Outline each blood parasite and name the species.
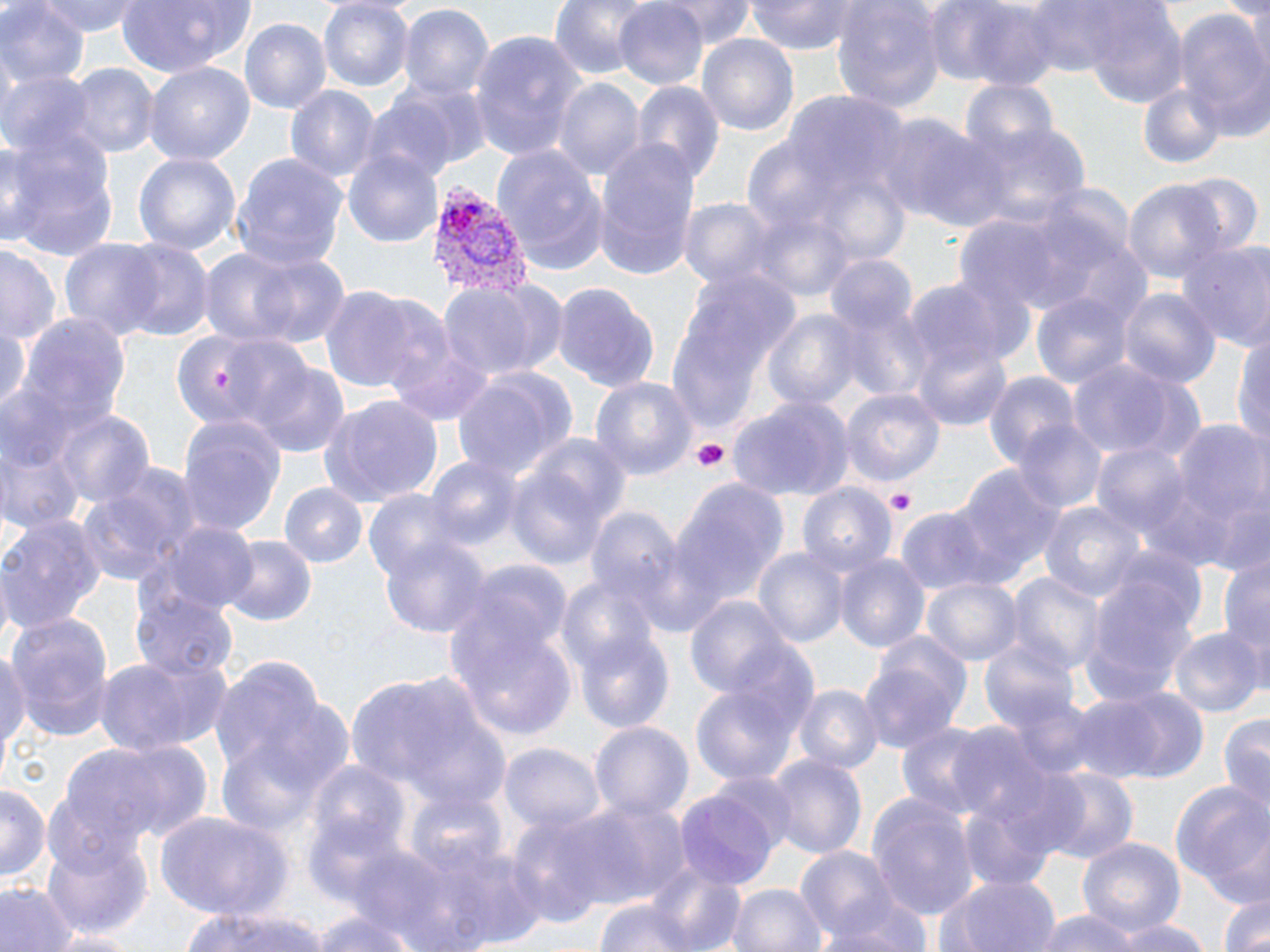
Approximate bounding boxes as named x1/y1/x2/y2 corners in pixels.
Plasmodium vivax-infected red blood cells: (x1=424, y1=182, x2=534, y2=306).
No Plasmodium falciparum, Plasmodium ovale, Plasmodium malariae, Babesia divergens, or Trypanosoma brucei observed.

Uninfected red blood cell locations: (x1=0, y1=0, x2=86, y2=95), (x1=40, y1=0, x2=142, y2=37), (x1=114, y1=0, x2=257, y2=78), (x1=549, y1=0, x2=665, y2=84), (x1=611, y1=0, x2=710, y2=91), (x1=657, y1=0, x2=757, y2=43), (x1=745, y1=0, x2=867, y2=52), (x1=831, y1=0, x2=945, y2=114), (x1=1019, y1=0, x2=1131, y2=77), (x1=1245, y1=0, x2=1269, y2=82), (x1=934, y1=1, x2=1063, y2=88), (x1=317, y1=2, x2=413, y2=91), (x1=399, y1=3, x2=494, y2=106), (x1=1082, y1=4, x2=1189, y2=111), (x1=1172, y1=8, x2=1270, y2=141), (x1=239, y1=17, x2=332, y2=115), (x1=469, y1=33, x2=585, y2=161), (x1=698, y1=33, x2=798, y2=141), (x1=145, y1=62, x2=255, y2=164), (x1=69, y1=66, x2=159, y2=157), (x1=0, y1=69, x2=95, y2=161), (x1=552, y1=77, x2=643, y2=182), (x1=960, y1=80, x2=1060, y2=162), (x1=632, y1=81, x2=724, y2=188), (x1=1135, y1=81, x2=1228, y2=172), (x1=287, y1=85, x2=380, y2=187), (x1=360, y1=96, x2=462, y2=185), (x1=875, y1=106, x2=1003, y2=232), (x1=962, y1=119, x2=1090, y2=229), (x1=0, y1=133, x2=123, y2=264), (x1=594, y1=140, x2=703, y2=281), (x1=492, y1=144, x2=611, y2=273), (x1=345, y1=150, x2=443, y2=250), (x1=134, y1=152, x2=241, y2=260), (x1=232, y1=153, x2=349, y2=271), (x1=1174, y1=172, x2=1263, y2=259), (x1=1122, y1=179, x2=1226, y2=285), (x1=677, y1=198, x2=776, y2=292), (x1=58, y1=239, x2=168, y2=337), (x1=115, y1=239, x2=213, y2=341), (x1=1174, y1=239, x2=1270, y2=352), (x1=201, y1=242, x2=344, y2=351), (x1=1, y1=243, x2=62, y2=350), (x1=664, y1=267, x2=804, y2=437), (x1=903, y1=275, x2=1031, y2=377), (x1=438, y1=281, x2=560, y2=382), (x1=550, y1=282, x2=661, y2=394), (x1=321, y1=287, x2=425, y2=397), (x1=1116, y1=288, x2=1220, y2=391), (x1=1032, y1=290, x2=1135, y2=393), (x1=764, y1=308, x2=867, y2=417), (x1=15, y1=314, x2=134, y2=445), (x1=0, y1=320, x2=32, y2=418), (x1=382, y1=327, x2=497, y2=428), (x1=1234, y1=330, x2=1270, y2=452), (x1=170, y1=333, x2=261, y2=428), (x1=221, y1=336, x2=316, y2=429), (x1=913, y1=341, x2=1014, y2=432), (x1=1065, y1=359, x2=1194, y2=460), (x1=250, y1=361, x2=350, y2=456), (x1=451, y1=369, x2=576, y2=483), (x1=987, y1=373, x2=1078, y2=471), (x1=591, y1=375, x2=697, y2=479), (x1=840, y1=387, x2=944, y2=486), (x1=317, y1=393, x2=442, y2=508), (x1=728, y1=394, x2=851, y2=500), (x1=53, y1=408, x2=155, y2=514), (x1=177, y1=413, x2=285, y2=537), (x1=1169, y1=416, x2=1270, y2=551), (x1=1012, y1=420, x2=1105, y2=515), (x1=1093, y1=440, x2=1194, y2=544), (x1=1, y1=445, x2=82, y2=534), (x1=424, y1=457, x2=521, y2=552), (x1=504, y1=459, x2=619, y2=575), (x1=79, y1=464, x2=204, y2=585), (x1=948, y1=465, x2=1063, y2=588), (x1=669, y1=474, x2=790, y2=616), (x1=799, y1=483, x2=895, y2=582), (x1=279, y1=484, x2=367, y2=568), (x1=363, y1=486, x2=463, y2=583), (x1=1038, y1=501, x2=1145, y2=608), (x1=588, y1=505, x2=682, y2=610), (x1=895, y1=507, x2=999, y2=595), (x1=0, y1=514, x2=108, y2=637), (x1=150, y1=519, x2=262, y2=614), (x1=377, y1=530, x2=494, y2=643), (x1=219, y1=536, x2=318, y2=628), (x1=753, y1=547, x2=848, y2=652), (x1=1220, y1=550, x2=1270, y2=668), (x1=835, y1=551, x2=929, y2=655), (x1=1079, y1=572, x2=1201, y2=709), (x1=1011, y1=574, x2=1102, y2=674), (x1=556, y1=575, x2=662, y2=686), (x1=923, y1=575, x2=1023, y2=666), (x1=131, y1=590, x2=237, y2=682), (x1=683, y1=595, x2=792, y2=705), (x1=6, y1=613, x2=116, y2=740), (x1=449, y1=616, x2=578, y2=741), (x1=977, y1=628, x2=1084, y2=753), (x1=1169, y1=629, x2=1262, y2=720), (x1=577, y1=630, x2=674, y2=731), (x1=863, y1=633, x2=972, y2=753), (x1=0, y1=649, x2=32, y2=774), (x1=92, y1=650, x2=232, y2=759), (x1=207, y1=656, x2=352, y2=819), (x1=345, y1=668, x2=511, y2=809), (x1=796, y1=684, x2=881, y2=774), (x1=693, y1=685, x2=798, y2=787), (x1=1067, y1=685, x2=1204, y2=783), (x1=1219, y1=709, x2=1270, y2=825), (x1=591, y1=721, x2=693, y2=826), (x1=897, y1=721, x2=995, y2=820), (x1=80, y1=736, x2=215, y2=845), (x1=501, y1=742, x2=603, y2=835), (x1=769, y1=755, x2=866, y2=859), (x1=306, y1=762, x2=410, y2=857), (x1=1038, y1=769, x2=1138, y2=866), (x1=1168, y1=781, x2=1265, y2=904), (x1=0, y1=784, x2=47, y2=887), (x1=405, y1=789, x2=509, y2=876), (x1=864, y1=791, x2=978, y2=920), (x1=676, y1=793, x2=778, y2=888), (x1=570, y1=799, x2=692, y2=911), (x1=960, y1=802, x2=1059, y2=893), (x1=153, y1=808, x2=294, y2=920), (x1=506, y1=811, x2=619, y2=925), (x1=303, y1=816, x2=416, y2=913), (x1=1075, y1=836, x2=1186, y2=936), (x1=40, y1=837, x2=153, y2=939), (x1=387, y1=837, x2=545, y2=952), (x1=798, y1=846, x2=899, y2=947), (x1=641, y1=864, x2=746, y2=949), (x1=935, y1=872, x2=1061, y2=952), (x1=1, y1=881, x2=74, y2=952), (x1=728, y1=884, x2=827, y2=952), (x1=1213, y1=888, x2=1270, y2=952), (x1=826, y1=895, x2=937, y2=952), (x1=593, y1=899, x2=702, y2=952), (x1=180, y1=904, x2=328, y2=952), (x1=306, y1=904, x2=427, y2=952), (x1=1032, y1=907, x2=1146, y2=952), (x1=1110, y1=916, x2=1208, y2=952), (x1=44, y1=929, x2=143, y2=952). Platelet locations: (x1=211, y1=367, x2=235, y2=396), (x1=694, y1=441, x2=730, y2=472), (x1=886, y1=489, x2=917, y2=515). Slide-level diagnosis: Plasmodium vivax. Light microscopy. Image is 1270×952 pixels. Thin blood smear. 1000x magnification. May-Grünwald-Giemsa stain. One field of a larger specimen.